Assess this cell for malaria.
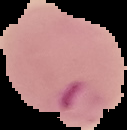
Parasitized.

image type = segmented cell region with the area outside set to black
preparation = thin blood film
image size = 127×130 pixels